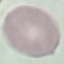
Malaria status: uninfected. Acquired by smartphone through the microscope eyepiece. Giemsa stain. Cell patch, automatically extracted from a larger field of view and resized to 64 × 64 pixels. Thin blood film.